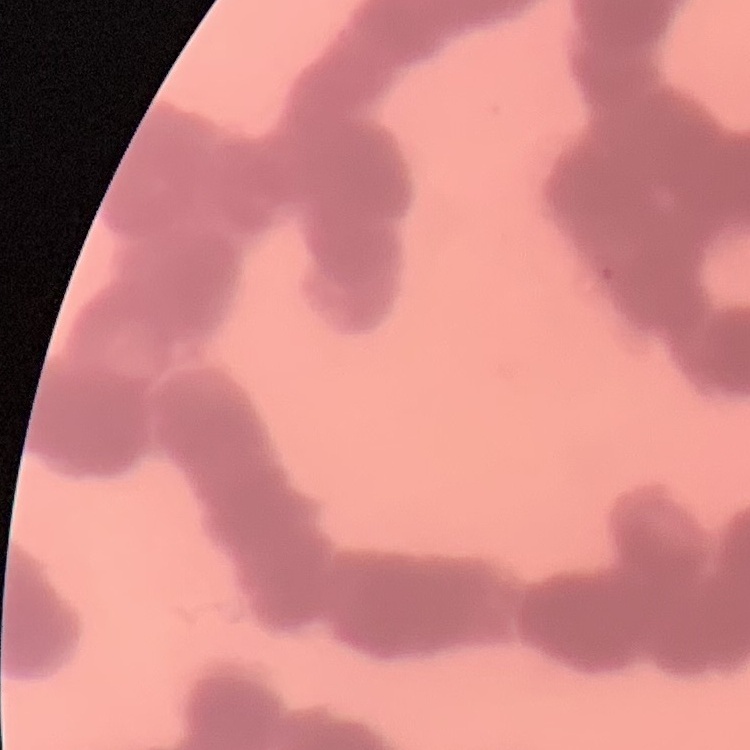 The red blood cells exhibit rouleaux formation. Thin peripheral smear. Stained with either Field's or Giemsa. One tile cut from a larger photomicrograph.